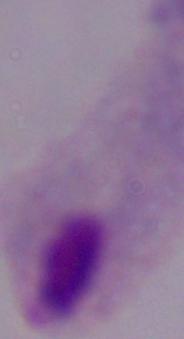

magnification = 1000x
identification = trichomonad
modality = photomicrograph